Comment on the morphology of the erythrocytes.
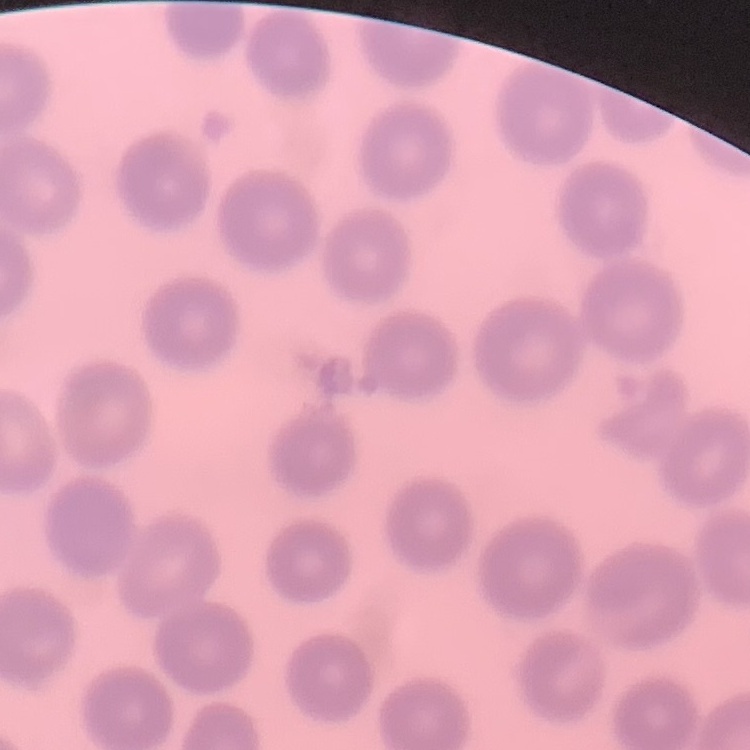

No rouleaux formation.

Summary:
  - Image type: one tile cut from a larger photomicrograph
  - Preparation: thin peripheral smear
  - Stain: Field's or Giemsa